Outline each blood parasite and name the species.
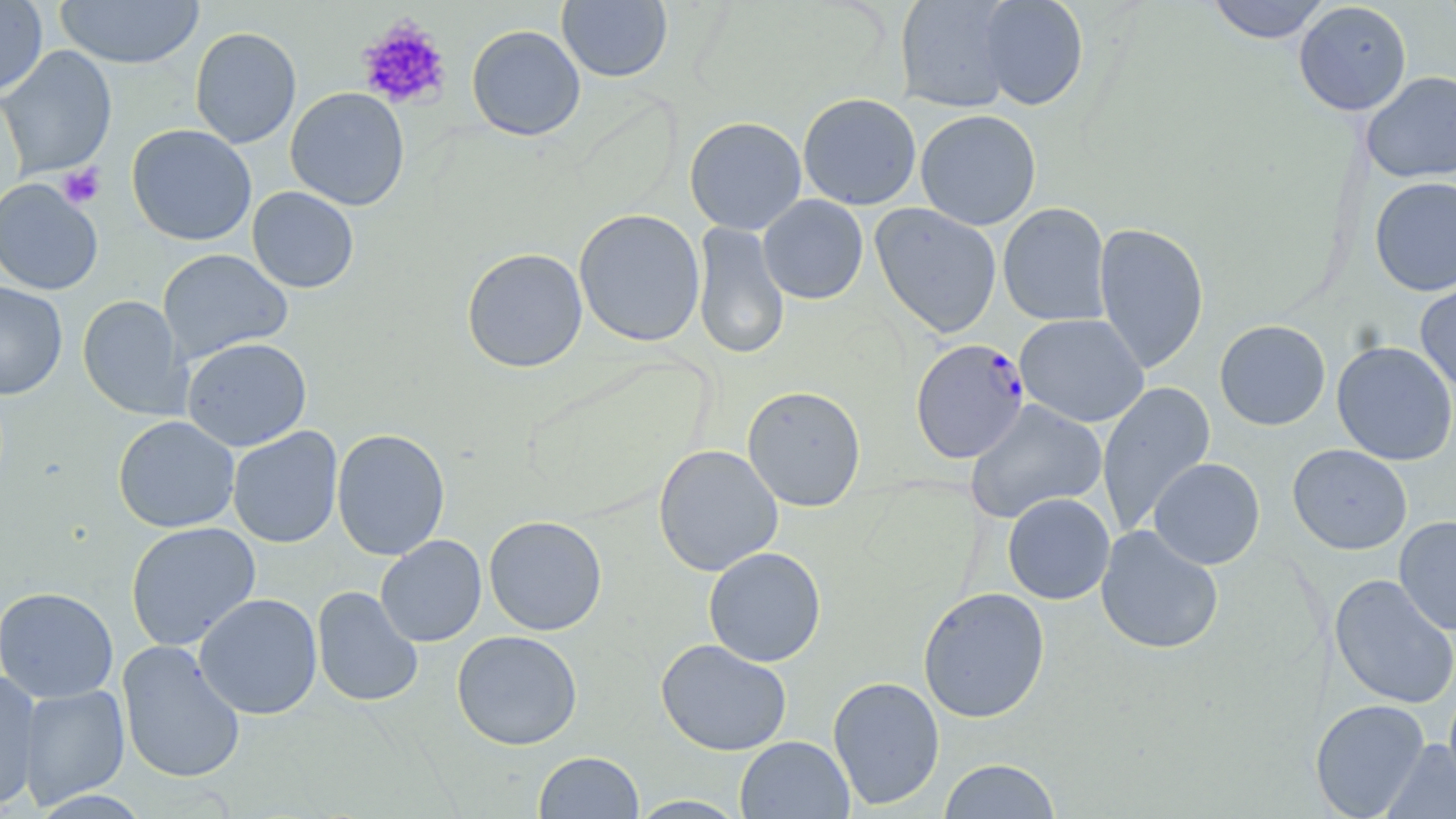
Approximate bounding boxes as (x1,y1)-(x2,y2) corner pairs in pixels.
Plasmodium falciparum-infected red blood cells: (909,338)-(1030,462).
No Plasmodium ovale, Plasmodium malariae, Plasmodium vivax, Babesia divergens, or Trypanosoma brucei observed.

Uninfected red blood cell locations: (55,0)-(204,69), (894,0)-(1019,113), (976,0)-(1089,110), (1205,0)-(1331,44), (0,1)-(48,97), (557,1)-(673,83), (1294,1)-(1412,116), (466,25)-(586,141), (189,26)-(302,149), (0,45)-(117,179), (1361,71)-(1456,183), (285,87)-(410,211), (798,92)-(921,210), (915,109)-(1041,230), (684,116)-(807,235), (126,124)-(257,246), (1369,176)-(1456,296), (1,178)-(103,296), (247,186)-(359,293), (757,195)-(869,304), (998,202)-(1112,327), (870,203)-(1002,338), (574,208)-(706,347), (692,221)-(790,361), (1093,222)-(1209,373), (461,247)-(588,373), (157,248)-(293,364), (1415,274)-(1456,395), (0,281)-(68,399), (77,295)-(189,419), (1015,313)-(1148,427), (1214,320)-(1331,431), (181,337)-(312,451), (1332,340)-(1456,466), (1096,381)-(1216,534), (742,385)-(866,511), (965,399)-(1107,523), (113,415)-(240,533), (228,427)-(343,548), (332,428)-(450,561), (653,444)-(783,576), (1287,444)-(1412,554), (1149,457)-(1265,570), (1002,493)-(1115,604), (484,515)-(607,635), (1394,515)-(1456,635), (125,521)-(261,650), (1095,525)-(1224,655), (376,535)-(487,646), (703,546)-(826,667), (1329,574)-(1456,709), (312,586)-(423,707), (0,587)-(119,703), (918,587)-(1050,722), (195,593)-(323,720), (451,630)-(583,750), (655,638)-(792,756), (117,640)-(246,784), (0,670)-(41,810), (827,675)-(945,810), (18,684)-(130,808), (1444,686)-(1456,793), (1310,699)-(1430,818), (735,735)-(854,819), (1381,739)-(1456,819), (534,751)-(644,818), (938,758)-(1061,818), (627,795)-(749,818). Platelet locations: (356,19)-(452,110), (57,163)-(106,209). Slide-level diagnosis: Plasmodium falciparum. One field of a larger specimen. May-Grünwald-Giemsa stain. Image is 1456×819 pixels. Thin blood smear. Captured at 1000x magnification. Light microscopy.